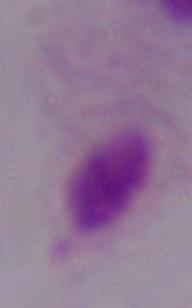
modality = photomicrograph
magnification = 1000x
identification = trichomonad